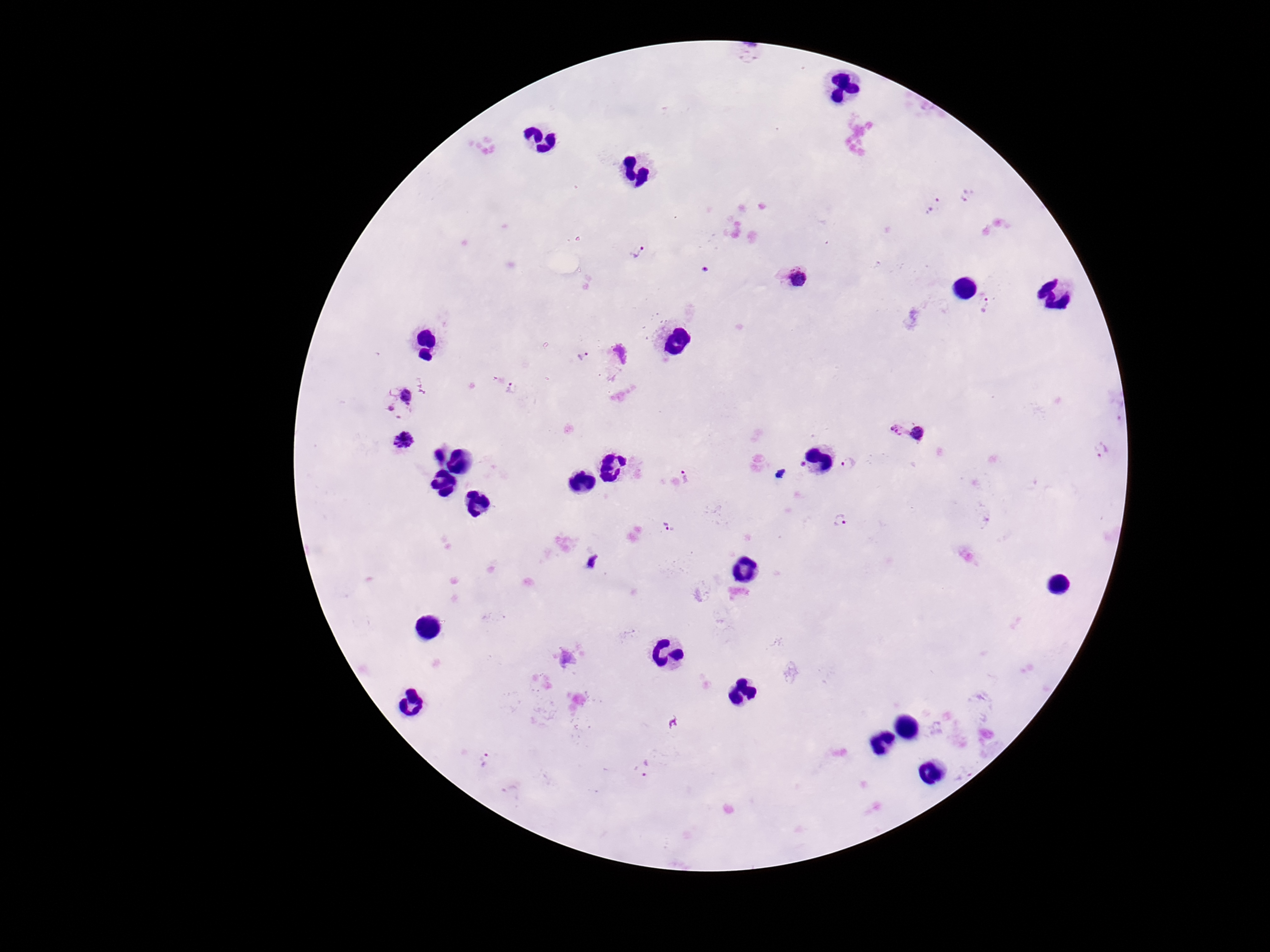
magnification = 100x
stain = Giemsa
preparation = thick peripheral-blood smear
capture = smartphone camera through the microscope eyepiece
Plasmodium parasite locations = approximate centers as {x, y} in pixels: {967, 195}, {933, 204}, {637, 251}, {799, 278}, {982, 302}, {621, 352}, {583, 355}, {512, 388}, {404, 398}, {898, 429}, {918, 433}, {403, 441}, {1101, 450}, {438, 455}, {847, 463}, {803, 465}, {684, 476}, {840, 520}, {666, 526}, {567, 659}, {485, 759}, {642, 768}, {509, 789}
image size = 1270×952 pixels
field of view = single
patient malaria status = positive